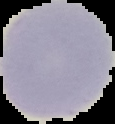
Summary:
  - Malaria status: uninfected
  - Preparation: thin blood smear
  - Image size: 115×124 pixels
  - Image type: cell region segmented out of the field of view; surrounding area masked to black